Name the blood parasite species.
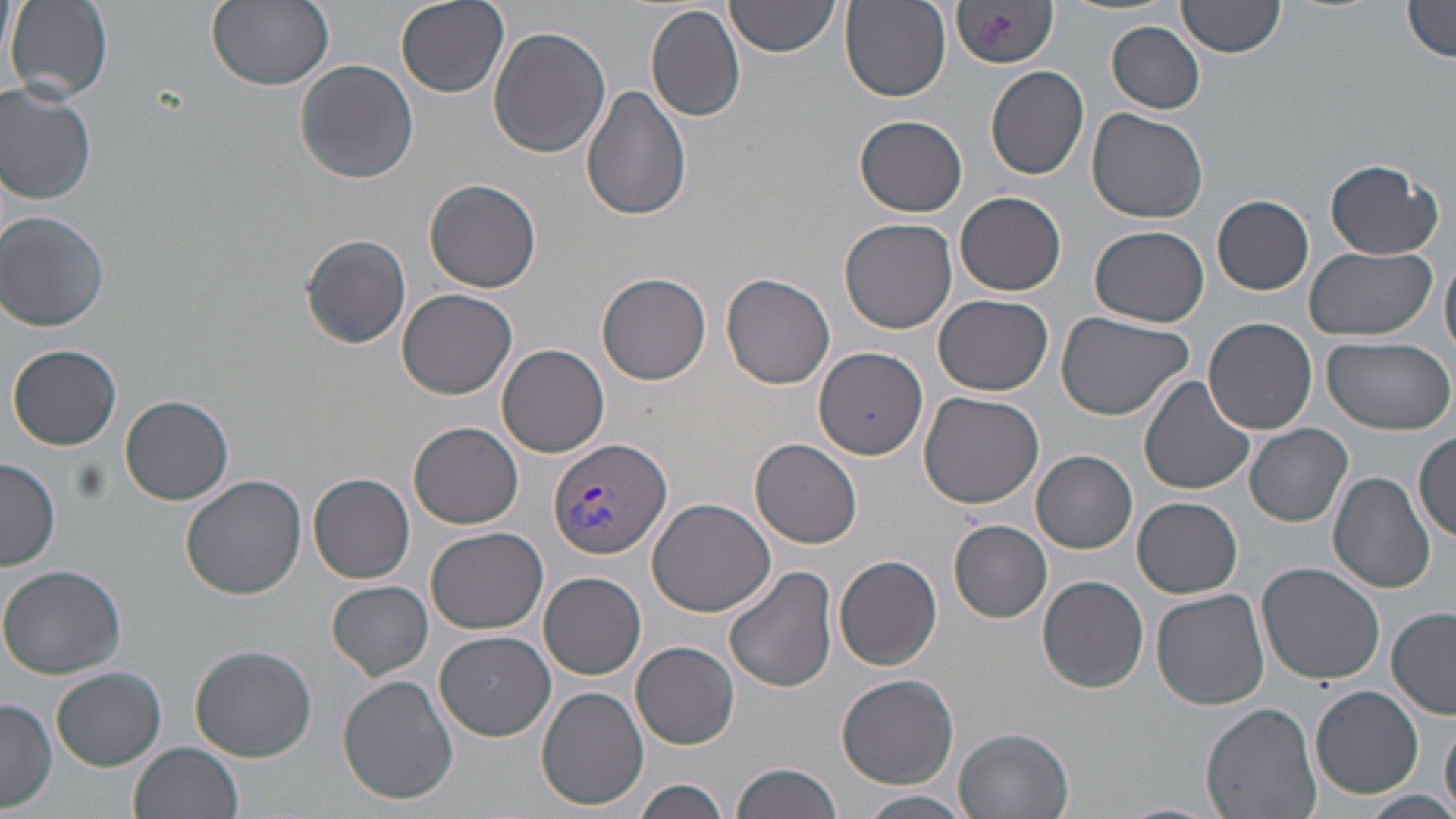

Plasmodium vivax.

Approximate bounding boxes as named x1/y1/x2/y2 corners in pixels. Uninfected red blood cell locations: (x1=3, y1=0, x2=26, y2=101), (x1=6, y1=0, x2=113, y2=103), (x1=207, y1=0, x2=334, y2=91), (x1=396, y1=0, x2=509, y2=98), (x1=725, y1=0, x2=838, y2=57), (x1=1179, y1=0, x2=1286, y2=57), (x1=950, y1=1, x2=1057, y2=70), (x1=1403, y1=1, x2=1456, y2=62), (x1=841, y1=2, x2=951, y2=102), (x1=645, y1=4, x2=747, y2=122), (x1=1107, y1=21, x2=1206, y2=114), (x1=488, y1=26, x2=612, y2=160), (x1=294, y1=61, x2=419, y2=185), (x1=986, y1=65, x2=1089, y2=180), (x1=0, y1=81, x2=99, y2=205), (x1=581, y1=85, x2=692, y2=222), (x1=1086, y1=108, x2=1209, y2=222), (x1=855, y1=114, x2=967, y2=217), (x1=1325, y1=161, x2=1443, y2=259), (x1=424, y1=179, x2=543, y2=293), (x1=955, y1=190, x2=1068, y2=295), (x1=1213, y1=195, x2=1313, y2=295), (x1=1, y1=211, x2=110, y2=331), (x1=840, y1=218, x2=958, y2=332), (x1=1091, y1=225, x2=1210, y2=326), (x1=300, y1=234, x2=412, y2=349), (x1=1305, y1=244, x2=1436, y2=341), (x1=1441, y1=254, x2=1456, y2=359), (x1=597, y1=273, x2=712, y2=386), (x1=721, y1=274, x2=835, y2=390), (x1=397, y1=288, x2=519, y2=399), (x1=933, y1=294, x2=1053, y2=396), (x1=1056, y1=312, x2=1195, y2=420), (x1=1204, y1=318, x2=1317, y2=436), (x1=1322, y1=336, x2=1453, y2=433), (x1=496, y1=343, x2=609, y2=458), (x1=9, y1=345, x2=121, y2=451), (x1=813, y1=347, x2=927, y2=458), (x1=1139, y1=376, x2=1255, y2=497), (x1=918, y1=392, x2=1044, y2=510), (x1=121, y1=394, x2=234, y2=505), (x1=409, y1=422, x2=524, y2=530), (x1=1245, y1=425, x2=1353, y2=528), (x1=1413, y1=430, x2=1456, y2=542), (x1=750, y1=439, x2=862, y2=548), (x1=1032, y1=451, x2=1137, y2=552), (x1=0, y1=457, x2=60, y2=570), (x1=1328, y1=471, x2=1436, y2=592), (x1=308, y1=473, x2=415, y2=583), (x1=181, y1=476, x2=308, y2=601), (x1=648, y1=497, x2=776, y2=617), (x1=1132, y1=497, x2=1243, y2=598), (x1=950, y1=521, x2=1052, y2=622), (x1=425, y1=525, x2=548, y2=636), (x1=834, y1=555, x2=943, y2=671), (x1=1255, y1=562, x2=1386, y2=686), (x1=0, y1=565, x2=129, y2=679), (x1=724, y1=566, x2=839, y2=695), (x1=539, y1=570, x2=646, y2=679), (x1=1037, y1=576, x2=1149, y2=693), (x1=327, y1=580, x2=433, y2=679), (x1=1151, y1=589, x2=1269, y2=713), (x1=1387, y1=609, x2=1456, y2=718), (x1=435, y1=630, x2=554, y2=741), (x1=631, y1=641, x2=739, y2=750), (x1=190, y1=643, x2=317, y2=763), (x1=52, y1=667, x2=167, y2=769), (x1=338, y1=673, x2=459, y2=807), (x1=837, y1=673, x2=959, y2=788), (x1=536, y1=685, x2=649, y2=812), (x1=1310, y1=686, x2=1425, y2=799), (x1=0, y1=699, x2=58, y2=811), (x1=1201, y1=701, x2=1322, y2=819), (x1=1442, y1=715, x2=1456, y2=814), (x1=955, y1=728, x2=1075, y2=819), (x1=129, y1=742, x2=244, y2=819), (x1=733, y1=761, x2=844, y2=819), (x1=633, y1=779, x2=731, y2=819), (x1=855, y1=790, x2=974, y2=819), (x1=1360, y1=790, x2=1454, y2=818). Plasmodium vivax-infected red blood cell locations: (x1=547, y1=437, x2=672, y2=560). Captured at 1000x magnification. Thin blood smear. One field of a larger specimen. Image is 1456×819 pixels. Optical microscopy. May-Grünwald-Giemsa stain.